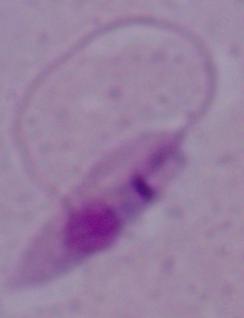

Summary:
  - Modality: micrograph
  - Magnification: 1000x
  - Identification: Leishmania